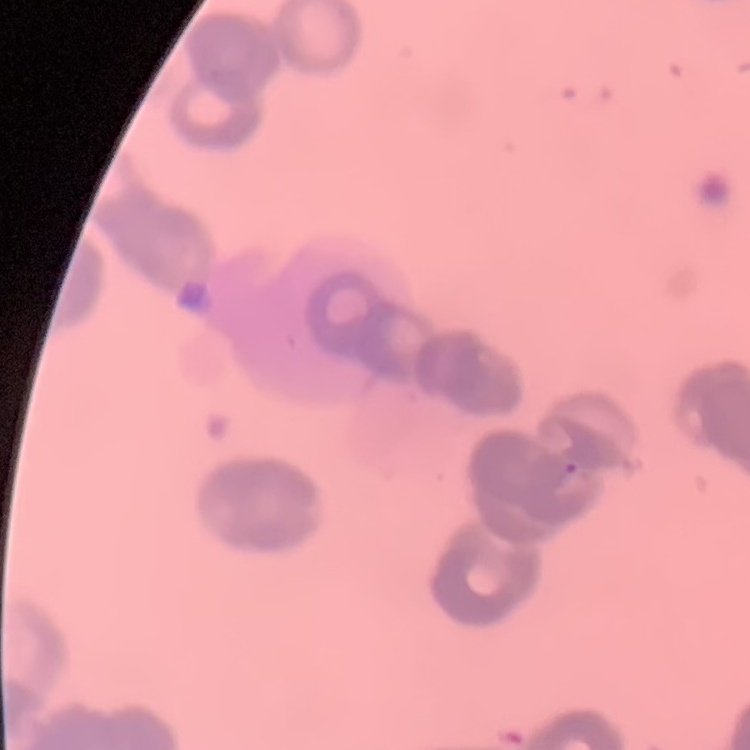 The red blood cells exhibit rouleaux formation. One tile cut from a larger photomicrograph. Thin blood film. Stained with either Field's or Giemsa.